Classify this cell by malaria status.
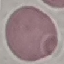
Uninfected.

Summary:
  - Capture: smartphone through the microscope eyepiece
  - Stain: Giemsa
  - Image type: cell patch, automatically extracted from a larger field of view and resized to 64 × 64 pixels
  - Preparation: thin blood smear